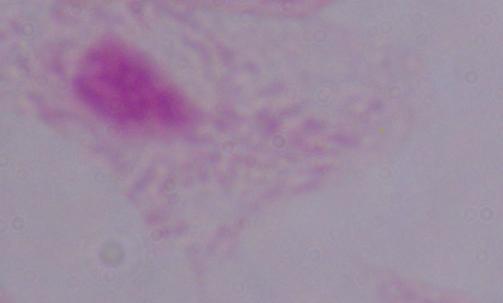
Summary:
  - Identification: trichomonad
  - Magnification: 1000x
  - Modality: micrograph